Identify the parasite.
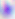

This is Toxoplasma gondii.

Micrograph. Captured at 400x magnification.